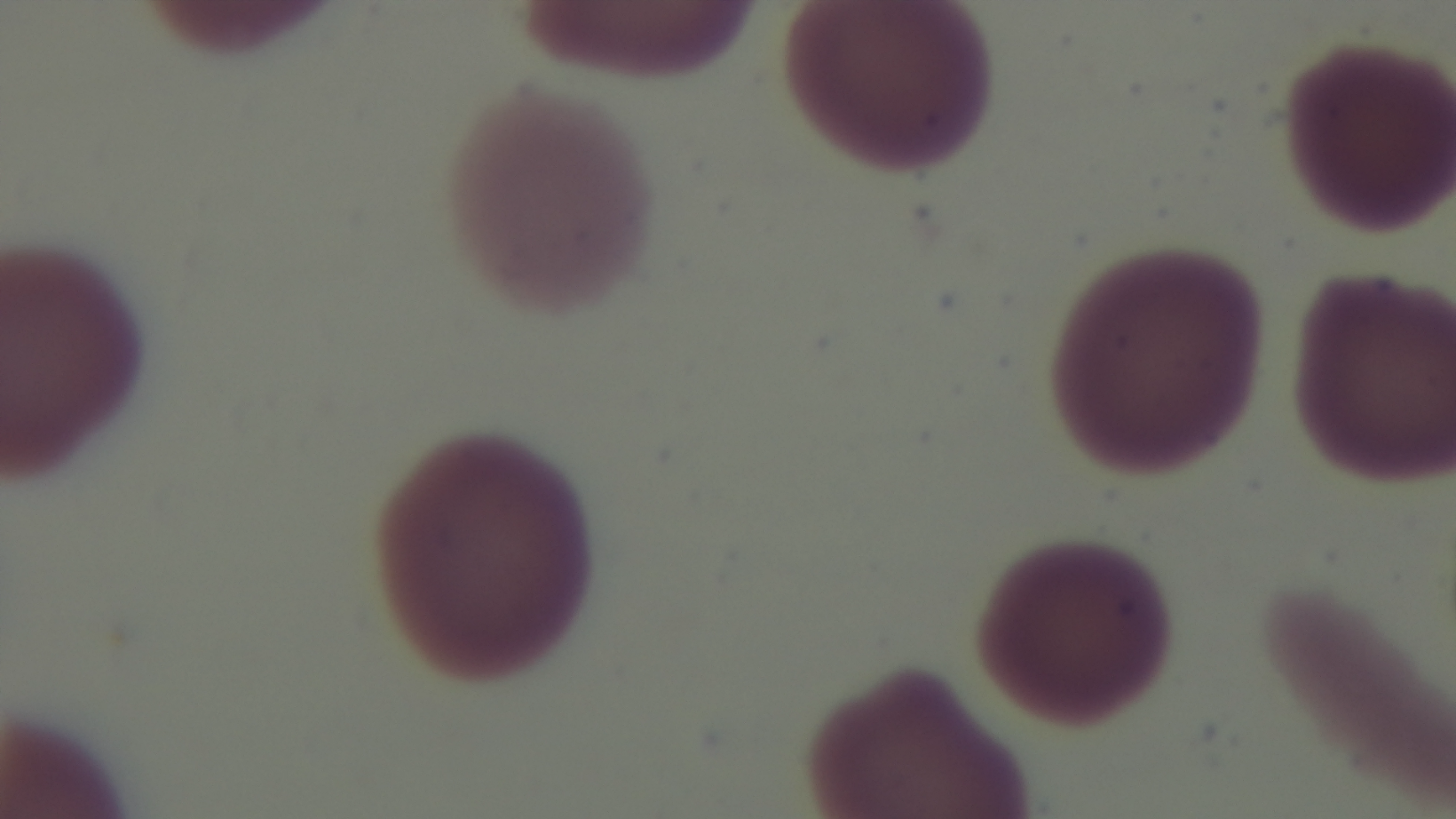

Summary:
  - Malaria status: negative
  - Objective: 100x oil immersion
  - Modality: light microscopy
  - Stain: Giemsa
  - Field of view: one from the slide
  - Preparation: thin blood film
  - Capture: mounted 4K digital camera